Describe the morphology of the erythrocytes.
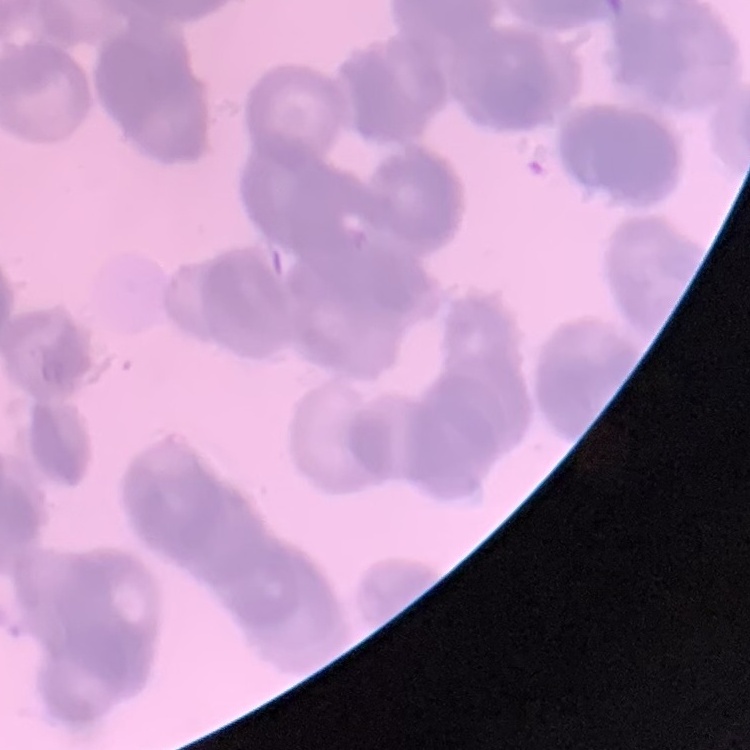
Rouleaux formation.

preparation = thin blood film
image type = square crop of a larger photomicrograph
stain = Field's or Giemsa